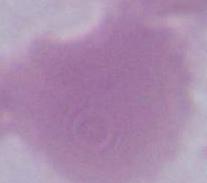

An erythrocyte is seen. Captured at 1000x magnification. Photomicrograph.